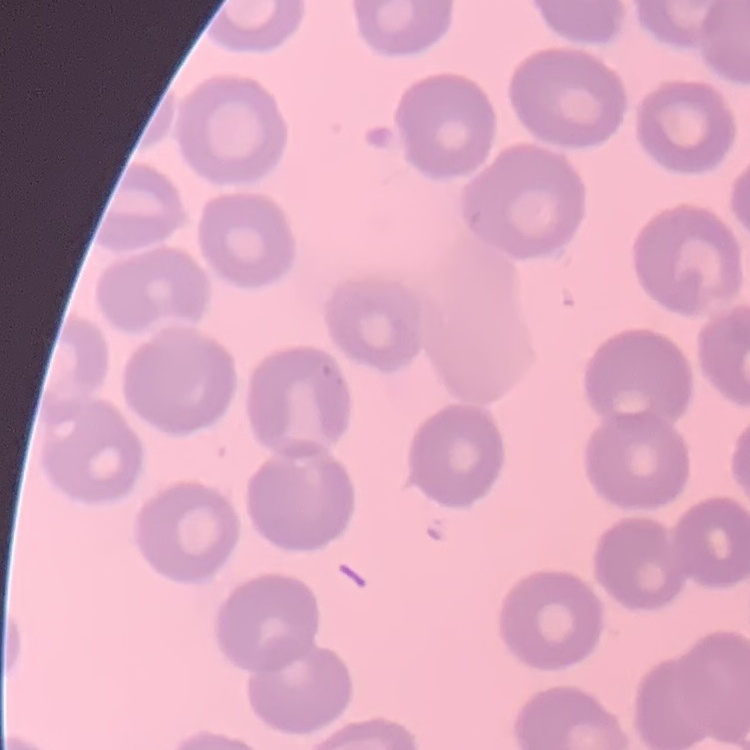
The red blood cells exhibit no rouleaux formation. Thin blood film. Field's or Giemsa stain. One tile cut from a larger photomicrograph.